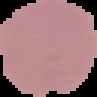

Summary:
  - Image type: segmented cell region with the area outside set to black
  - Malaria status: uninfected
  - Image size: 97×97 pixels
  - Preparation: thin blood smear